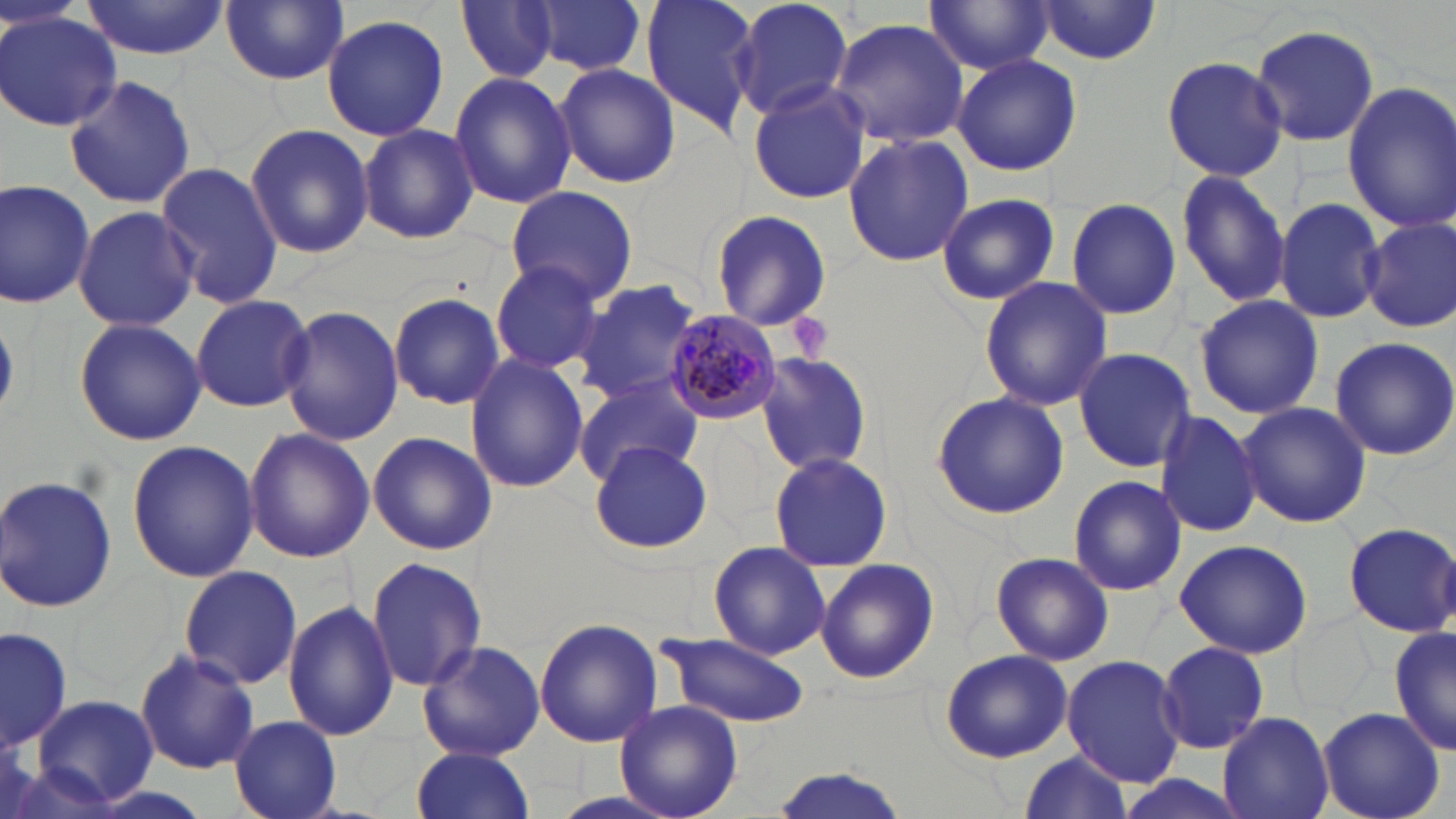
Approximate bounding boxes as [x1, y1, x2, y2] in pixels. Uninfected red blood cell locations: [81, 0, 229, 59], [220, 0, 349, 86], [527, 0, 647, 77], [642, 0, 763, 137], [730, 0, 854, 123], [925, 0, 1054, 74], [455, 2, 560, 84], [1033, 2, 1166, 65], [1, 12, 117, 130], [322, 13, 449, 141], [831, 17, 969, 147], [1247, 22, 1382, 148], [951, 53, 1082, 176], [1161, 55, 1287, 182], [555, 63, 680, 186], [448, 70, 577, 211], [64, 75, 196, 212], [748, 81, 872, 204], [1340, 82, 1455, 232], [358, 101, 569, 230], [358, 123, 480, 245], [246, 124, 373, 257], [844, 132, 972, 266], [153, 161, 284, 309], [1175, 169, 1291, 310], [0, 177, 97, 309], [504, 186, 639, 305], [936, 193, 1059, 305], [1063, 197, 1182, 322], [1274, 198, 1386, 323], [72, 205, 198, 331], [709, 209, 832, 330], [1358, 216, 1455, 333], [489, 260, 604, 373], [978, 276, 1112, 411], [572, 277, 703, 404], [189, 292, 314, 412], [388, 292, 506, 410], [1194, 293, 1323, 420], [279, 305, 403, 446], [74, 317, 205, 446], [1329, 337, 1456, 460], [1073, 347, 1197, 473], [465, 353, 588, 493], [757, 354, 874, 477], [574, 373, 702, 483], [931, 391, 1068, 520], [1235, 401, 1372, 529], [1154, 407, 1264, 539], [244, 427, 373, 563], [367, 431, 498, 555], [126, 440, 260, 582], [590, 440, 713, 555], [768, 451, 891, 571], [0, 472, 121, 617], [1068, 474, 1188, 596], [1343, 521, 1456, 638], [1173, 539, 1314, 659], [706, 542, 832, 660], [989, 550, 1113, 667], [366, 556, 488, 691], [815, 559, 940, 685], [179, 565, 302, 688], [286, 598, 396, 741], [534, 618, 662, 749], [1, 625, 73, 755], [1390, 626, 1455, 758], [658, 630, 811, 728], [417, 639, 547, 762], [1158, 641, 1269, 753], [941, 648, 1073, 763], [134, 649, 261, 774], [1062, 654, 1184, 787], [32, 694, 161, 808], [615, 699, 743, 819], [1313, 706, 1445, 819], [1217, 712, 1335, 819], [229, 715, 341, 819], [411, 746, 538, 819], [1014, 751, 1136, 818], [763, 766, 919, 819]. Platelet locations: [790, 309, 831, 363]. Plasmodium malariae-infected red blood cell locations: [664, 307, 782, 424]. Slide-level diagnosis: Plasmodium malariae. Single field of view. May-Grünwald-Giemsa stain. 1000x magnification. Thin blood smear. Image is 1456×819 pixels. Optical microscopy.